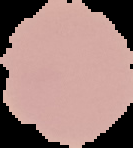
image size = 133×148 pixels
image type = cell region segmented out of the field of view; surrounding area masked to black
preparation = thin blood smear
result = no malaria parasites detected